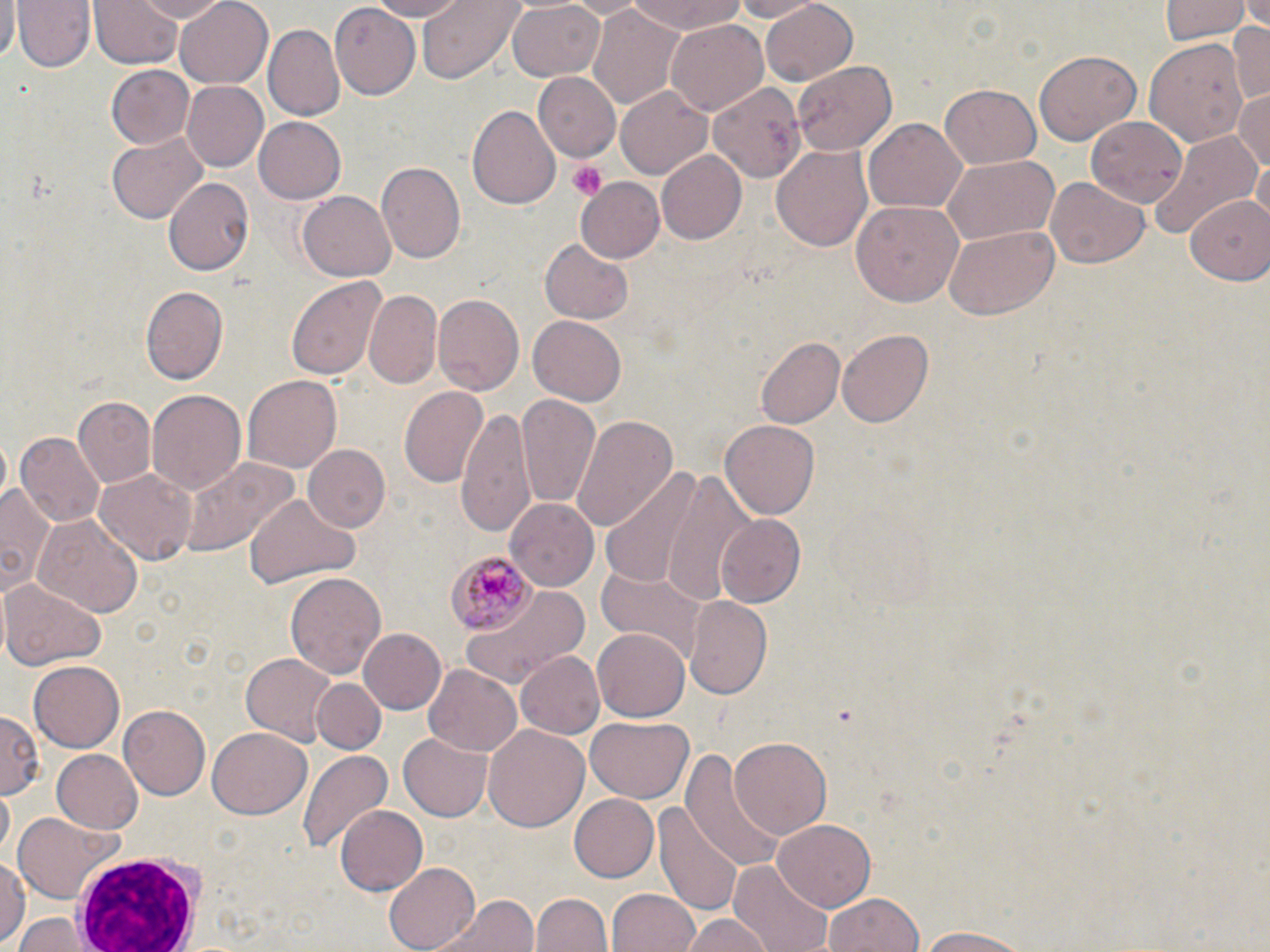
slide-level diagnosis = Plasmodium malariae
modality = light microscopy
Plasmodium malariae-infected red blood cell locations = approximate bounding boxes as [x1, y1, x2, y2] in pixels: [444, 552, 536, 635]
uninfected red blood cell locations = approximate bounding boxes as [x1, y1, x2, y2] in pixels: [0, 0, 18, 60], [14, 0, 94, 73], [127, 0, 233, 23], [175, 0, 274, 90], [362, 0, 474, 21], [417, 0, 521, 82], [625, 0, 747, 36], [728, 0, 820, 21], [1159, 0, 1250, 45], [91, 1, 183, 69], [505, 1, 607, 81], [331, 2, 421, 101], [757, 3, 859, 86], [589, 6, 689, 111], [1228, 18, 1270, 105], [665, 19, 769, 115], [266, 24, 345, 119], [1146, 37, 1248, 150], [1034, 49, 1142, 146], [793, 60, 899, 152], [104, 66, 195, 149], [534, 74, 621, 162], [181, 81, 269, 171], [708, 81, 806, 185], [939, 83, 1043, 167], [615, 84, 714, 180], [1233, 87, 1270, 175], [468, 105, 561, 211], [1088, 113, 1188, 204], [254, 118, 344, 204], [863, 119, 966, 215], [1148, 129, 1258, 241], [106, 132, 207, 224], [771, 145, 873, 252], [657, 150, 749, 245], [1251, 153, 1269, 224], [941, 158, 1059, 244], [375, 163, 465, 265], [1045, 177, 1149, 269], [165, 178, 254, 276], [575, 178, 665, 261], [298, 192, 396, 280], [1184, 196, 1270, 284], [852, 200, 967, 305], [945, 226, 1058, 318], [540, 238, 633, 324], [286, 275, 388, 379], [139, 284, 227, 384], [363, 292, 441, 392], [433, 294, 522, 397], [527, 315, 626, 407], [836, 329, 931, 429], [755, 335, 844, 428], [242, 374, 342, 476], [399, 384, 488, 490], [146, 390, 246, 495], [518, 396, 603, 510], [74, 397, 156, 488], [455, 406, 536, 535], [572, 413, 678, 529], [720, 420, 818, 520], [12, 432, 104, 528], [301, 445, 391, 533], [179, 456, 299, 558], [95, 465, 197, 565], [599, 467, 711, 594], [655, 467, 762, 601], [0, 479, 54, 597], [247, 492, 359, 588], [507, 498, 598, 588], [31, 512, 144, 618], [715, 514, 809, 608], [598, 564, 705, 662], [285, 570, 385, 680], [1, 577, 106, 670], [462, 584, 594, 684], [684, 596, 772, 701], [359, 627, 448, 715], [592, 628, 690, 721], [516, 651, 604, 740], [238, 655, 338, 746], [29, 659, 125, 750], [422, 665, 523, 757], [313, 678, 385, 754], [119, 705, 210, 801], [0, 711, 39, 799], [585, 716, 693, 805], [484, 724, 590, 832], [207, 727, 311, 819], [399, 734, 492, 819], [731, 736, 831, 838], [296, 746, 394, 852], [685, 747, 790, 874], [52, 749, 144, 834], [567, 794, 658, 882], [656, 799, 744, 918], [333, 803, 426, 897], [12, 812, 128, 905], [774, 819, 878, 912], [0, 855, 26, 948], [383, 861, 482, 951], [733, 861, 834, 952], [608, 887, 700, 952], [436, 893, 538, 952], [534, 893, 611, 952], [823, 893, 924, 952], [15, 914, 91, 951], [680, 914, 772, 952], [915, 926, 1039, 950]
stain = May-Grünwald-Giemsa
field of view = single
preparation = thin blood smear
white blood cell locations = approximate bounding boxes as [x1, y1, x2, y2] in pixels: [74, 847, 207, 952]
image size = 1270×952 pixels
platelet locations = approximate bounding boxes as [x1, y1, x2, y2] in pixels: [567, 161, 608, 199]
magnification = 1000x